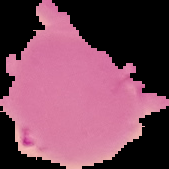 The area outside the segmented cell region is set to black. From a thin blood film. Image is 169×169 pixels. Result: no malaria parasites detected.